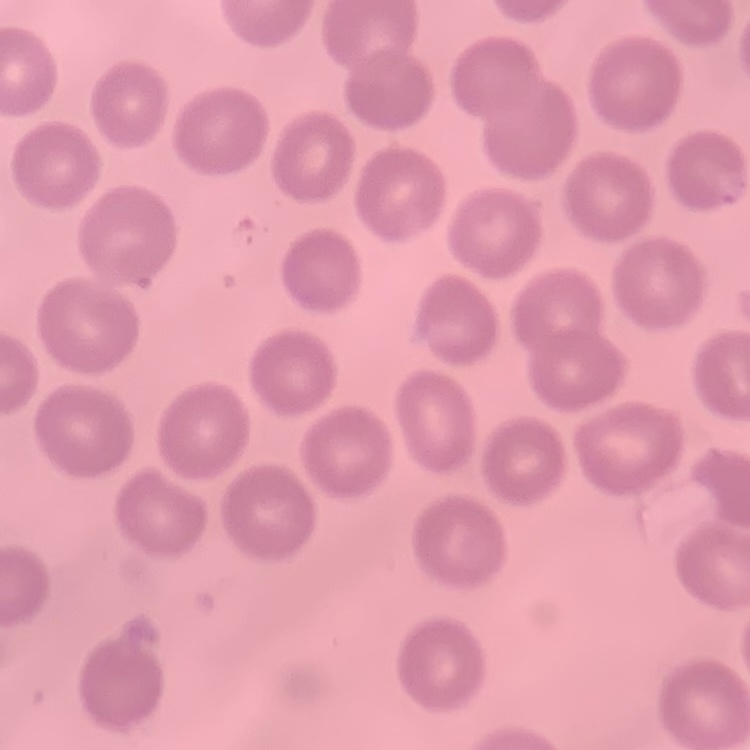

The red blood cells exhibit no rouleaux formation. Thin blood smear. Stained with either Field's or Giemsa. Square crop of a larger photomicrograph.